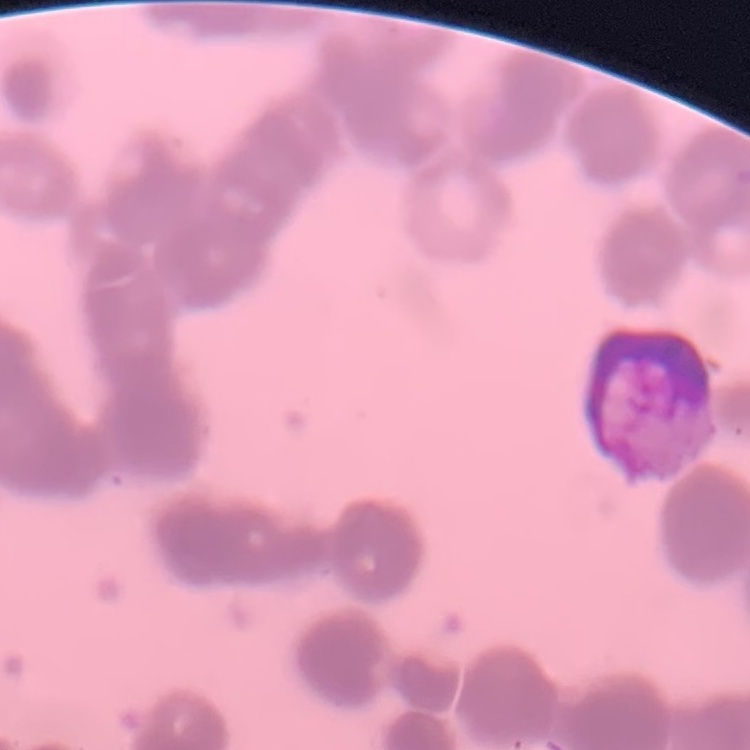
The red blood cells show rouleaux formation. One tile cut from a larger photomicrograph. Thin blood film. Field's or Giemsa stain.